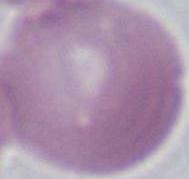
Micrograph. An erythrocyte is shown. Captured at 1000x magnification.